Give a bounding box for every malaria parasite, every leukocyte, and every artifact (stain precipitate or debris).
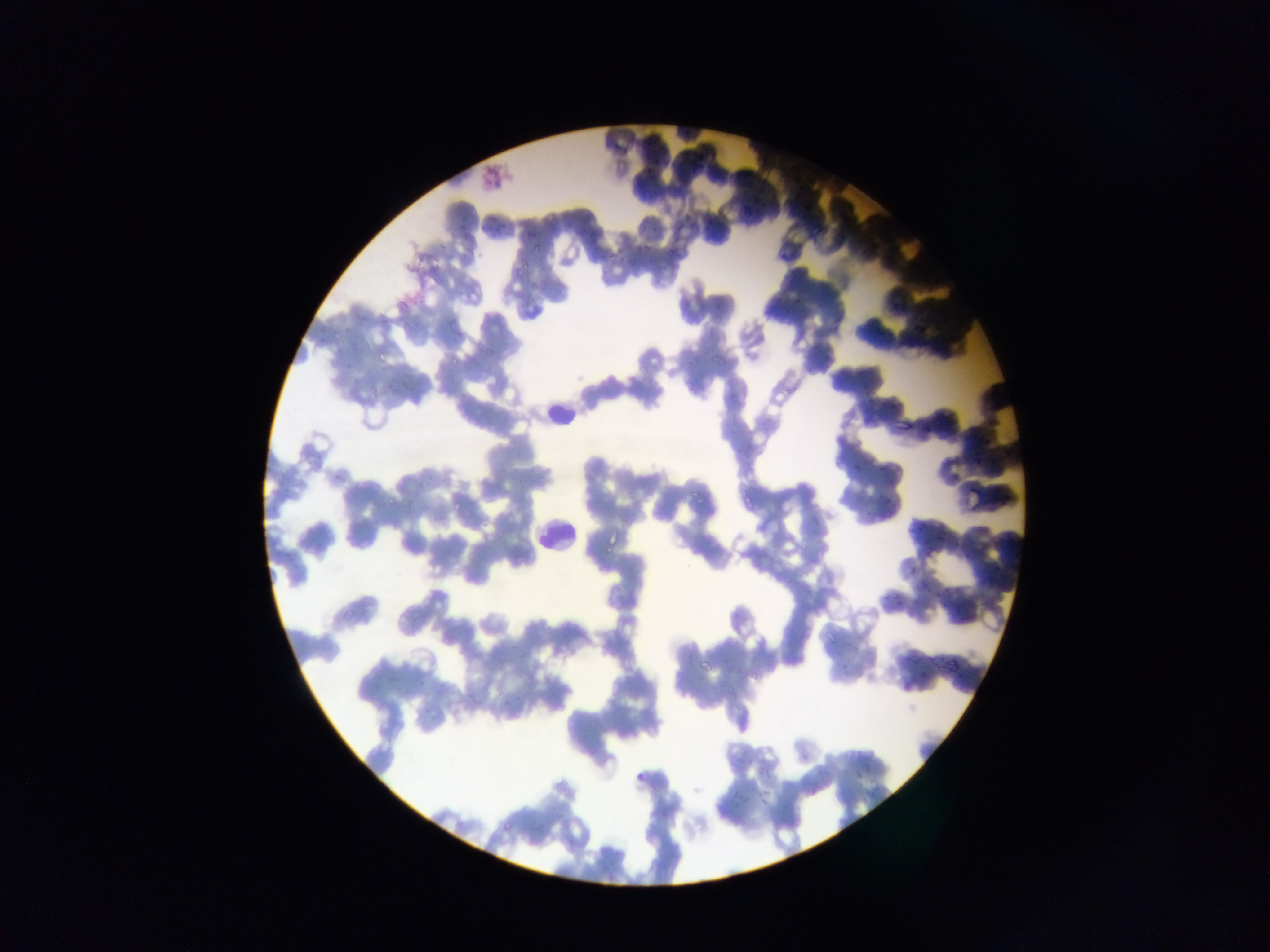

Approximate bounding boxes as [left, top, right, bottom] in pixels.
Malaria parasites: [608, 129, 627, 159], [646, 151, 661, 178], [741, 197, 766, 215], [456, 208, 472, 238], [682, 210, 695, 220], [491, 213, 502, 234], [522, 222, 538, 240], [648, 226, 660, 232], [667, 234, 693, 257], [613, 236, 626, 261], [531, 241, 543, 257], [636, 244, 650, 262], [514, 251, 533, 278], [594, 255, 608, 277], [714, 293, 730, 311], [332, 323, 357, 345], [376, 340, 397, 363], [711, 345, 736, 363], [444, 356, 459, 366], [340, 362, 352, 371], [369, 381, 380, 391], [866, 395, 875, 402], [891, 409, 909, 433], [851, 455, 862, 472], [877, 464, 889, 474], [949, 470, 963, 484], [735, 485, 753, 509], [692, 487, 709, 505], [386, 488, 399, 506], [450, 494, 465, 512], [881, 495, 892, 505], [883, 498, 891, 524], [808, 508, 819, 522], [913, 522, 923, 536], [603, 534, 620, 553], [900, 557, 918, 571], [918, 575, 932, 594], [888, 582, 903, 604], [425, 592, 455, 614], [938, 596, 951, 607], [865, 648, 876, 656], [903, 649, 921, 663], [697, 651, 720, 672], [940, 661, 953, 676], [839, 663, 856, 678], [723, 670, 741, 694], [902, 670, 924, 688], [422, 711, 436, 727], [849, 761, 870, 785], [751, 766, 773, 781], [727, 786, 752, 814], [863, 789, 876, 801], [501, 804, 523, 833].
Leukocytes: [549, 402, 578, 430], [537, 518, 573, 551].

Summary:
  - Preparation: thin blood film
  - Field of view: single
  - Image size: 1270×952 pixels
  - Capture: mobile-phone photograph through a microscope
  - Country: Ghana